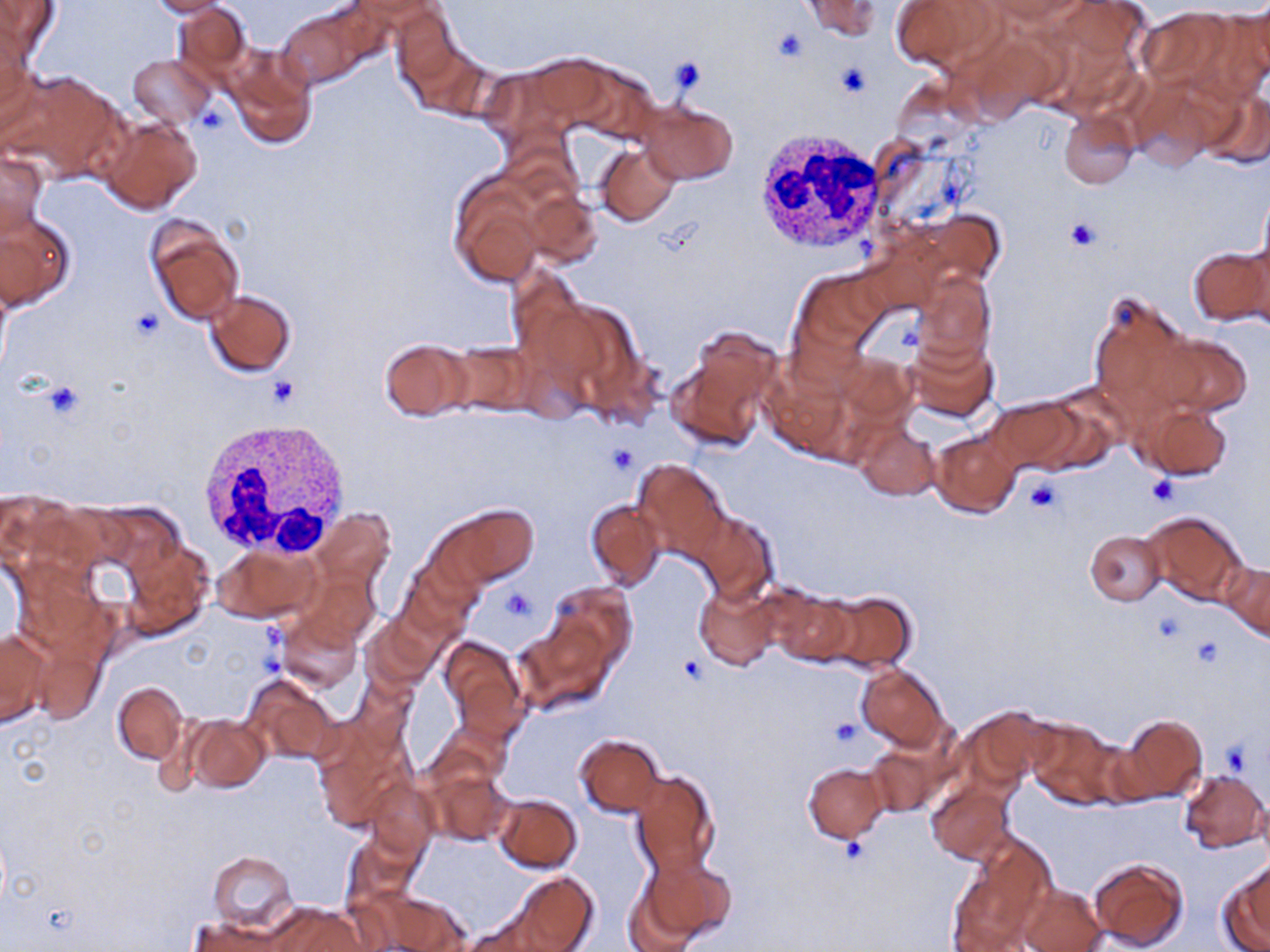
slide-level diagnosis = no evidence of blood parasites
white blood cell locations = approximate bounding boxes as [x1, y1, x2, y2] in pixels: [755, 128, 886, 253], [193, 416, 352, 561]
magnification = 1000x
uninfected red blood cell locations = approximate bounding boxes as [x1, y1, x2, y2] in pixels: [143, 0, 233, 17], [802, 0, 880, 41], [888, 0, 999, 72], [0, 1, 61, 57], [986, 1, 1093, 29], [1036, 1, 1148, 107], [170, 3, 252, 85], [275, 4, 383, 85], [1136, 8, 1239, 92], [389, 9, 465, 97], [0, 27, 34, 130], [225, 46, 316, 149], [129, 54, 215, 128], [3, 67, 119, 180], [1197, 86, 1270, 168], [637, 98, 738, 186], [1059, 112, 1138, 188], [97, 115, 204, 216], [597, 144, 680, 227], [0, 150, 48, 236], [448, 173, 548, 287], [1256, 184, 1270, 287], [520, 185, 603, 269], [0, 210, 76, 311], [144, 217, 245, 325], [1188, 246, 1268, 326], [797, 270, 888, 354], [913, 275, 995, 368], [206, 290, 296, 377], [1088, 291, 1196, 419], [673, 328, 783, 448], [1148, 329, 1256, 419], [900, 333, 999, 424], [381, 340, 472, 420], [446, 343, 536, 417], [836, 352, 919, 427], [760, 360, 856, 463], [986, 398, 1085, 474], [1134, 400, 1233, 480], [856, 422, 940, 499], [930, 428, 1023, 517], [633, 458, 729, 560], [585, 498, 666, 591], [443, 503, 537, 587], [688, 508, 778, 601], [314, 509, 395, 589], [1140, 511, 1246, 606], [1084, 530, 1166, 606], [124, 539, 214, 637], [216, 544, 318, 622], [398, 559, 481, 640], [1224, 561, 1270, 642], [303, 571, 380, 647], [547, 581, 636, 672], [694, 581, 781, 671], [764, 583, 854, 666], [819, 592, 915, 673], [279, 612, 361, 693], [364, 616, 436, 692], [518, 621, 612, 710], [1, 628, 51, 727], [32, 634, 107, 726], [439, 635, 526, 731], [857, 665, 946, 751], [241, 675, 337, 764], [112, 682, 187, 764], [955, 706, 1046, 791], [185, 715, 269, 791], [1121, 715, 1207, 802], [1026, 718, 1123, 806], [576, 734, 665, 816], [866, 745, 942, 817], [803, 763, 888, 841], [423, 765, 512, 848], [1179, 768, 1268, 852], [629, 771, 720, 877], [367, 780, 436, 858], [927, 782, 1014, 864], [493, 794, 582, 873], [951, 838, 1057, 950], [208, 849, 298, 933], [641, 853, 736, 944], [1087, 856, 1189, 951], [1220, 866, 1270, 952], [511, 872, 598, 952], [622, 873, 707, 952], [1017, 884, 1106, 952], [373, 891, 469, 951], [267, 905, 371, 952], [191, 916, 289, 952]
image size = 1270×952 pixels
stain = May-Grünwald-Giemsa
modality = optical microscopy
preparation = thin blood smear
field of view = one of a larger specimen
platelet locations = approximate bounding boxes as [x1, y1, x2, y2] in pixels: [771, 28, 810, 66], [667, 57, 706, 95], [834, 62, 872, 99], [193, 104, 230, 136], [1065, 218, 1100, 251], [267, 377, 300, 409], [40, 379, 85, 421], [607, 443, 637, 474], [1147, 474, 1177, 506], [1024, 475, 1064, 515], [502, 588, 536, 621], [1192, 637, 1224, 669], [678, 654, 706, 685], [830, 719, 860, 748], [1221, 740, 1252, 775], [840, 836, 870, 864]